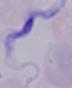

{
  "identification": "trypanosome",
  "magnification": "1000x",
  "modality": "photomicrograph"
}